Locate every blood parasite and identify its species.
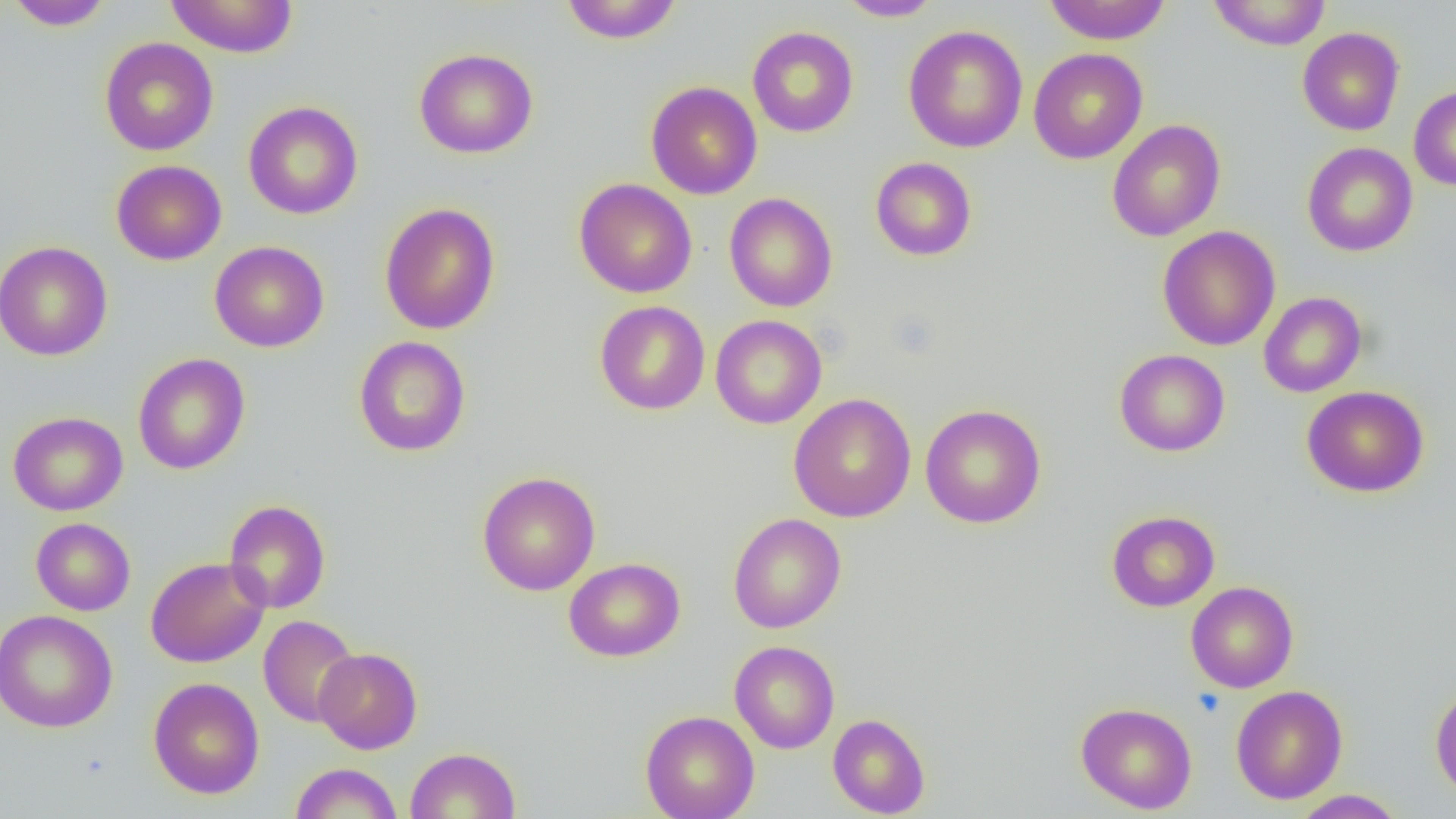
No blood parasites observed.

Summary:
  - Coordinate format: approximate bounding boxes as (x1,y1)-(x2,y2) corner pairs in pixels
  - Platelet locations: (1192,687)-(1226,718)
  - Uninfected red blood cell locations: (5,0)-(114,30), (164,0)-(299,58), (560,0)-(683,44), (837,0)-(944,21), (1206,0)-(1332,50), (1042,1)-(1173,45), (903,24)-(1028,153), (747,26)-(859,137), (1297,27)-(1405,136), (100,37)-(219,156), (414,48)-(538,159), (1029,48)-(1147,164), (645,81)-(762,199), (1408,85)-(1456,191), (243,101)-(363,220), (1107,119)-(1226,242), (1302,141)-(1418,257), (870,157)-(977,261), (111,160)-(226,266), (574,178)-(697,298), (724,193)-(837,312), (379,203)-(500,334), (1157,225)-(1280,351), (209,240)-(330,352), (0,241)-(113,361), (1259,291)-(1367,397), (595,301)-(710,415), (710,315)-(826,429), (353,336)-(471,457), (1115,349)-(1230,457), (132,352)-(250,475), (1302,386)-(1430,498), (788,393)-(916,522), (920,403)-(1046,528), (8,411)-(128,516), (477,471)-(600,595), (224,500)-(331,614), (1106,510)-(1219,612), (728,513)-(846,634), (31,517)-(136,616), (145,556)-(269,668), (564,558)-(685,662), (1186,581)-(1299,693), (0,609)-(118,733), (258,615)-(360,727), (729,640)-(840,753), (314,648)-(422,754), (148,677)-(265,799), (1430,683)-(1456,800), (1231,685)-(1347,804), (1076,701)-(1197,814), (641,710)-(759,819), (828,713)-(930,818), (405,747)-(521,819), (289,763)-(402,819), (1291,790)-(1406,818)
  - Slide-level diagnosis: no evidence of blood parasites
  - Preparation: thin blood smear
  - Magnification: 1000x
  - Image size: 1456×819 pixels
  - Modality: optical microscopy
  - Field of view: one of a larger specimen